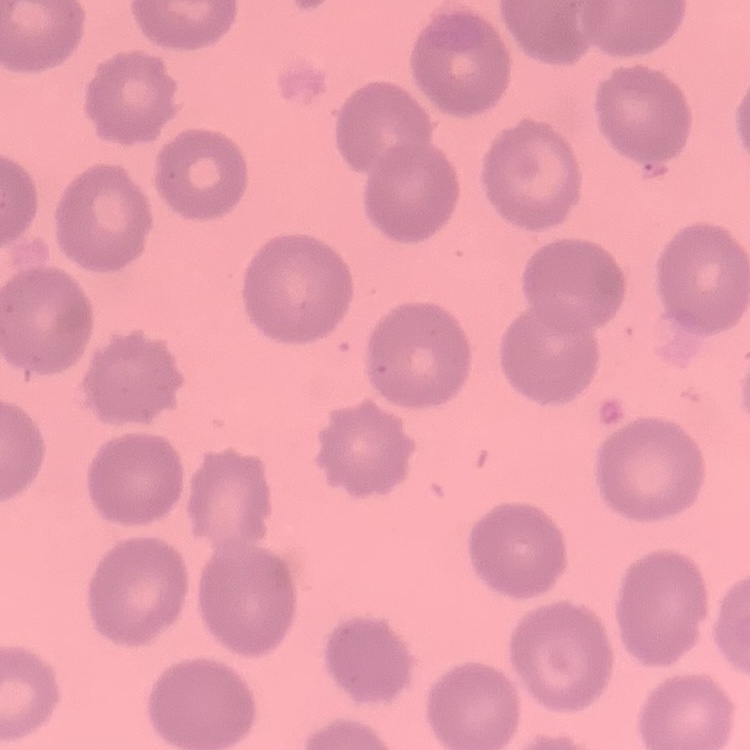

red blood cell morphology = no rouleaux formation
image type = square crop of a larger photomicrograph
preparation = thin blood film
stain = Field's or Giemsa